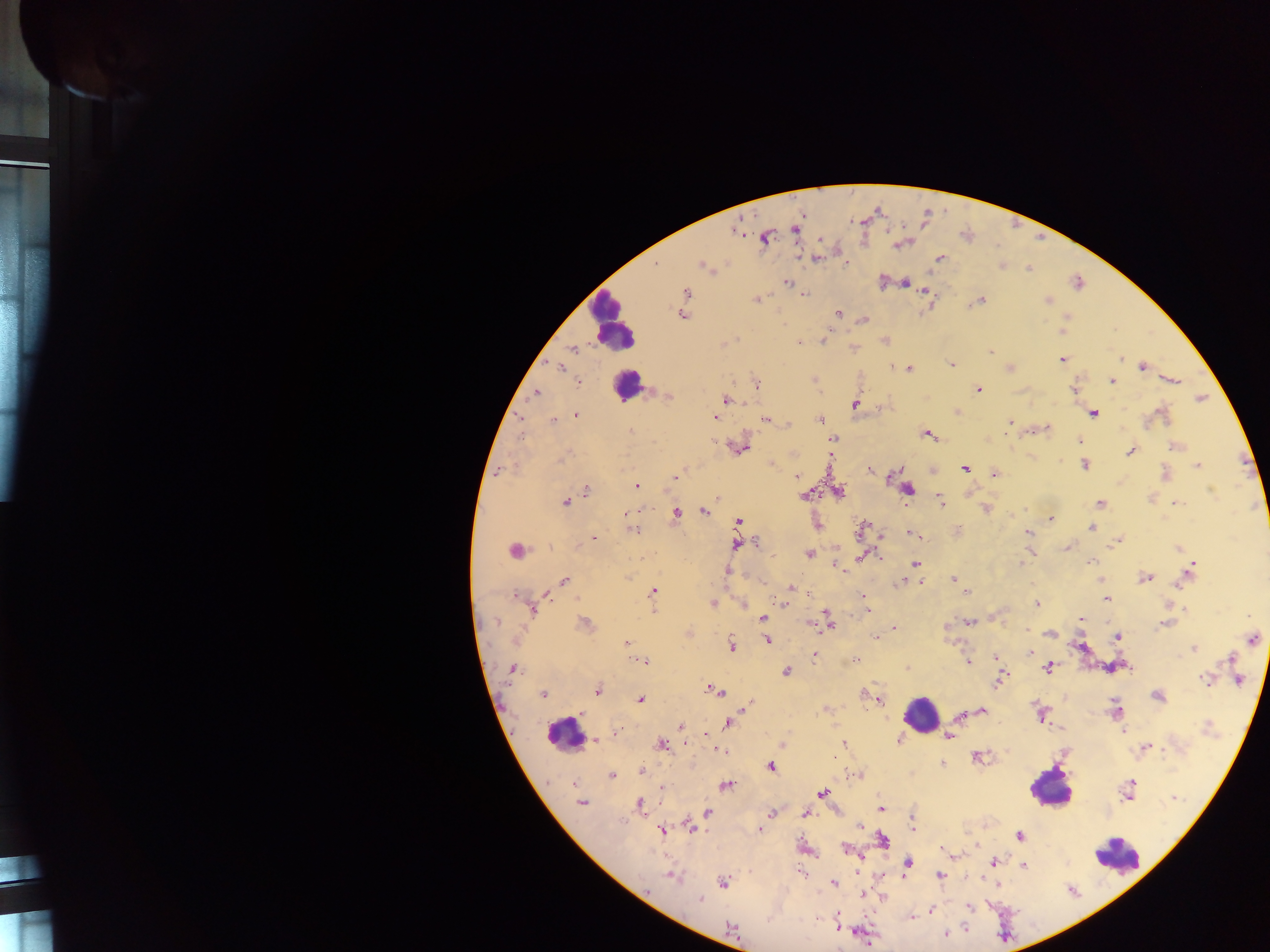 Approximate centers as {x, y} in pixels. Malaria parasite locations: {795, 229}, {737, 230}, {765, 237}, {901, 244}, {816, 258}, {939, 258}, {845, 263}, {654, 265}, {1002, 265}, {705, 266}, {1029, 267}, {883, 281}, {787, 282}, {904, 282}, {926, 290}, {685, 292}, {805, 293}, {756, 299}, {980, 300}, {1047, 300}, {837, 313}, {681, 314}, {1066, 317}, {864, 319}, {1061, 329}, {884, 340}, {822, 341}, {723, 343}, {799, 343}, {852, 347}, {572, 349}, {990, 352}, {1061, 359}, {1120, 359}, {950, 364}, {560, 366}, {1142, 366}, {1009, 368}, {909, 369}, {814, 379}, {1112, 380}, {1170, 380}, {578, 382}, {755, 383}, {977, 390}, {1074, 390}, {535, 393}, {668, 395}, {1200, 398}, {725, 400}, {855, 403}, {879, 408}, {956, 411}, {1093, 413}, {575, 415}, {1161, 415}, {715, 417}, {765, 419}, {820, 419}, {553, 420}, {1009, 422}, {788, 425}, {1045, 428}, {631, 433}, {928, 434}, {832, 439}, {1079, 440}, {1175, 446}, {738, 447}, {1129, 451}, {792, 454}, {830, 457}, {772, 464}, {1084, 465}, {1197, 465}, {965, 468}, {869, 469}, {499, 471}, {1165, 473}, {994, 474}, {675, 476}, {796, 476}, {637, 486}, {907, 489}, {586, 491}, {838, 492}, {806, 494}, {969, 494}, {717, 497}, {938, 499}, {564, 501}, {1175, 502}, {1098, 503}, {986, 508}, {703, 510}, {676, 512}, {626, 513}, {1050, 518}, {737, 522}, {1091, 527}, {632, 529}, {862, 529}, {957, 531}, {915, 534}, {1029, 534}, {882, 536}, {594, 537}, {1118, 539}, {757, 542}, {1114, 542}, {737, 544}, {1068, 547}, {1177, 548}, {1030, 550}, {515, 551}, {808, 553}, {877, 555}, {862, 556}, {1089, 562}, {915, 564}, {836, 565}, {1020, 565}, {725, 571}, {1187, 574}, {1144, 578}, {953, 579}, {1100, 579}, {564, 581}, {761, 581}, {903, 582}, {919, 582}, {790, 588}, {965, 591}, {653, 592}, {806, 592}, {863, 597}, {1106, 599}, {712, 603}, {743, 603}, {785, 603}, {864, 603}, {1036, 604}, {1168, 604}, {532, 608}, {653, 608}, {1185, 609}, {866, 612}, {762, 618}, {1081, 618}, {828, 621}, {969, 621}, {1168, 622}, {585, 624}, {894, 629}, {1027, 631}, {688, 633}, {1050, 633}, {1117, 636}, {1251, 638}, {875, 639}, {767, 640}, {627, 644}, {730, 645}, {1081, 647}, {1193, 647}, {1030, 652}, {814, 655}, {995, 656}, {1232, 659}, {854, 660}, {643, 661}, {968, 661}, {1048, 667}, {907, 668}, {511, 669}, {786, 671}, {1001, 678}, {1207, 678}, {1238, 680}, {997, 682}, {597, 690}, {714, 690}, {542, 694}, {866, 694}, {1157, 696}, {641, 699}, {879, 700}, {744, 704}, {826, 709}, {981, 710}, {1115, 710}, {1041, 714}, {958, 715}, {728, 723}, {680, 727}, {1123, 731}, {616, 732}, {704, 735}, {949, 735}, {594, 740}, {899, 740}, {661, 744}, {784, 744}, {843, 744}, {1145, 747}, {720, 751}, {978, 756}, {941, 765}, {771, 766}, {641, 771}, {859, 775}, {611, 776}, {575, 783}, {725, 785}, {663, 788}, {1128, 789}, {821, 793}, {581, 802}, {639, 805}, {880, 808}, {707, 812}, {772, 812}, {804, 813}, {912, 825}, {691, 826}, {758, 829}, {661, 830}, {1019, 835}, {882, 841}, {977, 845}, {942, 847}, {846, 848}, {955, 855}, {908, 862}, {994, 862}, {1023, 865}, {671, 875}, {940, 875}, {879, 876}, {723, 882}, {833, 883}, {996, 883}, {860, 894}, {883, 898}, {699, 900}, {968, 906}, {931, 910}, {910, 916}, {835, 921}, {730, 929}, {945, 933}. Leukocyte locations: {610, 322}, {625, 384}, {922, 715}, {564, 734}, {1051, 787}, {1116, 854}. Sample from Ghana. One field of view. Thick blood film. Mobile-phone photograph taken through the microscope. Image is 1270×952 pixels.